Report the malaria status of this cell.
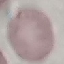
It is uninfected.

Photographed with a smartphone camera at the microscope eyepiece. Thin blood smear. Giemsa stain. Automatically extracted cell patch, resized to 64 × 64 pixels.